Report the malaria status of this cell.
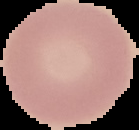

Uninfected.

The area outside the segmented cell region is set to black. Image is 139×130 pixels. From a thin blood smear.